Report the malaria status of this cell.
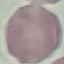

Uninfected.

Summary:
  - Stain: Giemsa
  - Preparation: thin blood smear
  - Capture: smartphone camera at the microscope eyepiece
  - Image type: cell patch, automatically extracted from a larger field of view and resized to 64 × 64 pixels